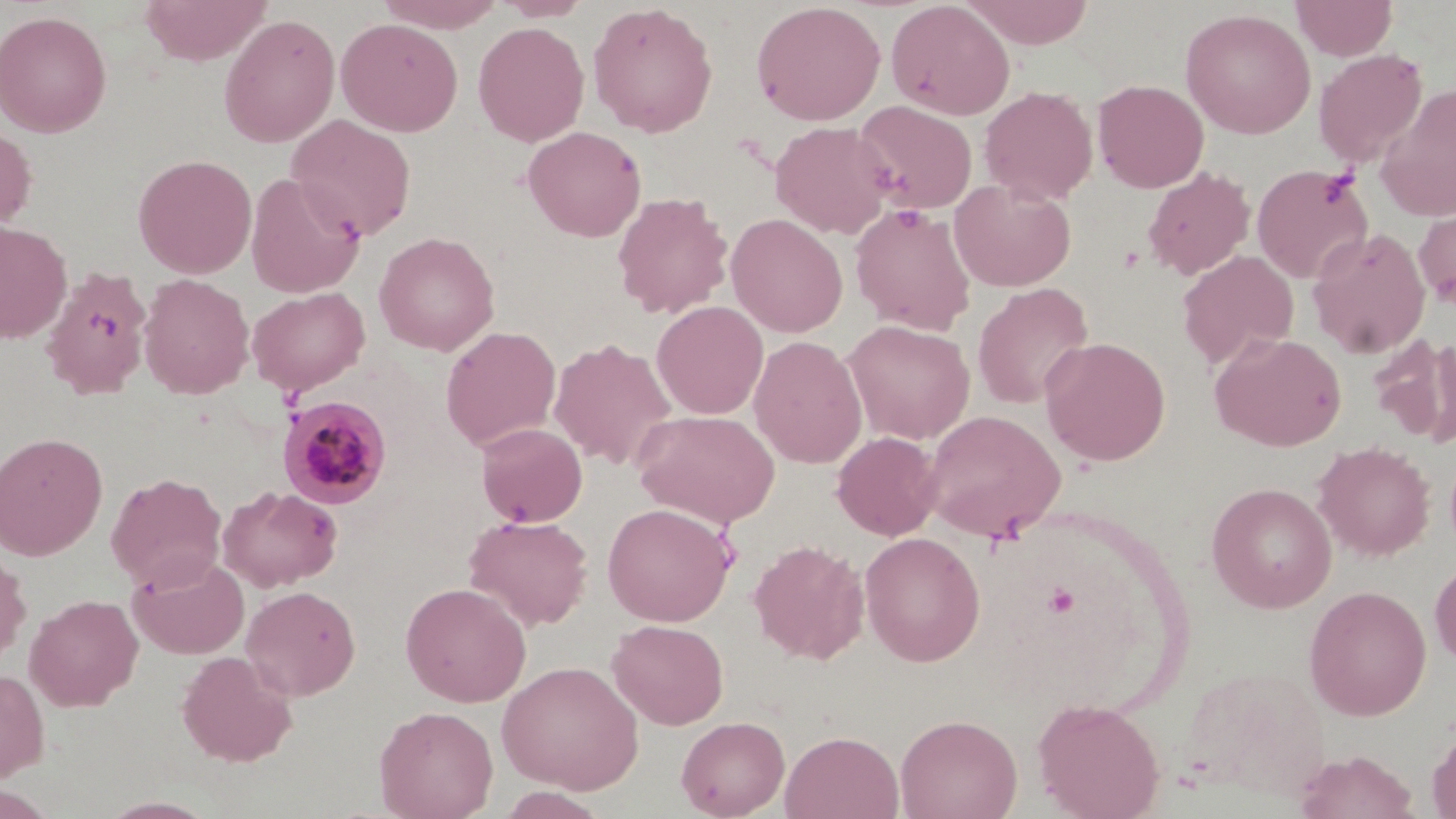 Approximate bounding boxes as [x1, y1, x2, y2] in pixels. Platelet locations: [1319, 171, 1358, 208]. Plasmodium malariae-infected red blood cell locations: [277, 394, 393, 509]. Uninfected red blood cell locations: [139, 0, 273, 65], [375, 0, 508, 32], [494, 0, 592, 21], [885, 0, 1016, 120], [962, 0, 1095, 48], [1291, 0, 1398, 61], [587, 2, 719, 137], [750, 2, 886, 125], [1180, 8, 1316, 139], [0, 9, 112, 137], [219, 13, 341, 148], [336, 17, 463, 137], [473, 22, 589, 147], [1313, 49, 1428, 168], [1093, 79, 1209, 193], [1376, 84, 1456, 223], [979, 85, 1098, 205], [854, 101, 978, 214], [286, 115, 417, 242], [769, 121, 894, 238], [0, 123, 37, 234], [523, 125, 646, 242], [134, 154, 257, 278], [1251, 164, 1375, 284], [1141, 167, 1255, 280], [245, 172, 365, 298], [949, 178, 1077, 292], [612, 192, 733, 319], [1414, 202, 1456, 310], [849, 203, 977, 335], [726, 213, 848, 338], [0, 221, 72, 343], [1307, 227, 1431, 359], [373, 232, 500, 355], [1177, 251, 1299, 369], [41, 268, 152, 398], [138, 273, 254, 399], [972, 282, 1095, 409], [246, 287, 370, 396], [651, 301, 768, 419], [842, 319, 976, 445], [441, 326, 561, 451], [1210, 332, 1347, 451], [1369, 334, 1456, 446], [749, 335, 867, 469], [1040, 336, 1171, 466], [549, 338, 678, 471], [632, 408, 780, 527], [922, 409, 1066, 542], [475, 423, 587, 527], [832, 431, 942, 540], [0, 432, 108, 561], [1314, 442, 1434, 561], [106, 472, 226, 591], [1207, 482, 1337, 613], [218, 485, 343, 592], [602, 502, 737, 627], [464, 514, 593, 631], [859, 531, 986, 666], [749, 539, 869, 664], [0, 544, 31, 670], [128, 554, 249, 659], [1429, 557, 1456, 667], [400, 582, 532, 707], [242, 585, 361, 700], [1303, 585, 1432, 720], [25, 594, 143, 710], [607, 619, 729, 730], [176, 650, 298, 766], [496, 659, 644, 794], [1181, 666, 1331, 801], [0, 667, 50, 782], [1032, 697, 1166, 818], [374, 705, 499, 819], [895, 713, 1022, 819], [675, 715, 790, 819], [1427, 724, 1456, 819], [780, 731, 904, 819], [1293, 750, 1419, 819]. Slide-level diagnosis: Plasmodium malariae. Thin blood film. Image is 1456×819 pixels. Single field of view. May-Grünwald-Giemsa-stained preparation. 1000x magnification. Light microscopy.